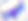

magnification = 400x
modality = photomicrograph
identification = Toxoplasma gondii